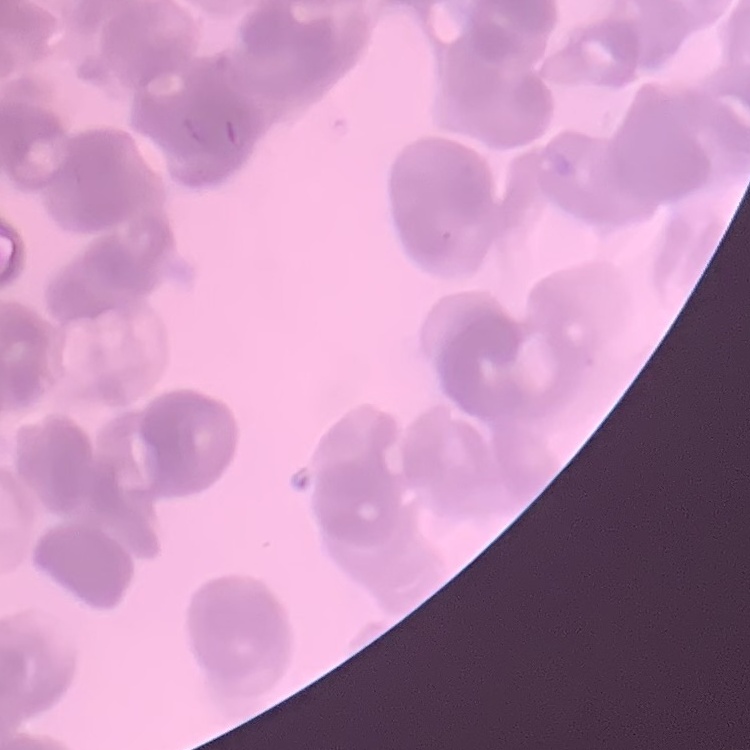
{
  "red_blood_cell_morphology": "rouleaux formation",
  "stain": "Field's or Giemsa",
  "image_type": "one tile cut from a larger photomicrograph",
  "preparation": "thin blood film"
}